Assess the morphology of the red blood cells.
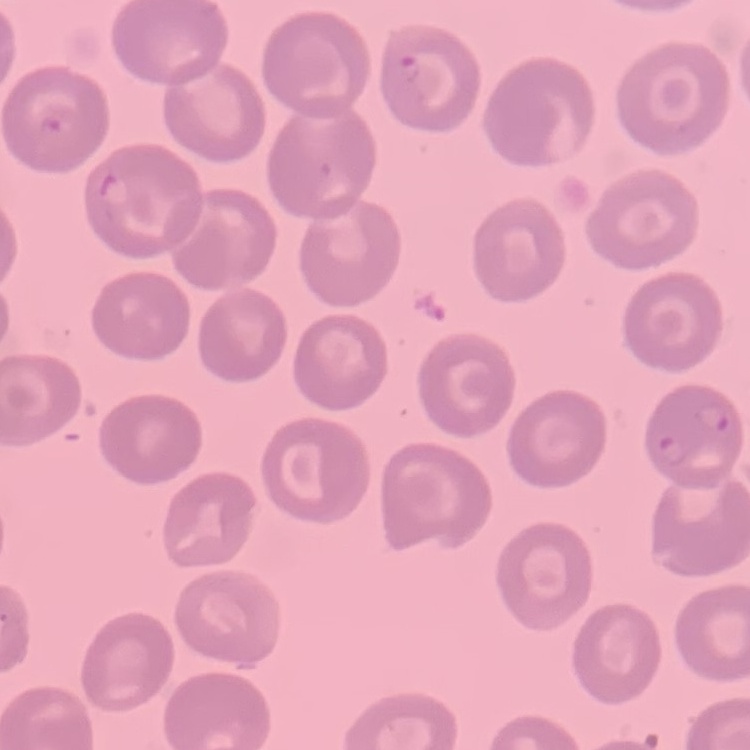

No rouleaux formation.

Stained with either Field's or Giemsa. Thin blood film. One tile cut from a larger photomicrograph.